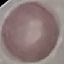 Result: no malaria parasites seen. Acquired by smartphone through the microscope eyepiece. Giemsa stain. Thin smear of blood. Automatically extracted cell patch, resized to 64 × 64 pixels.